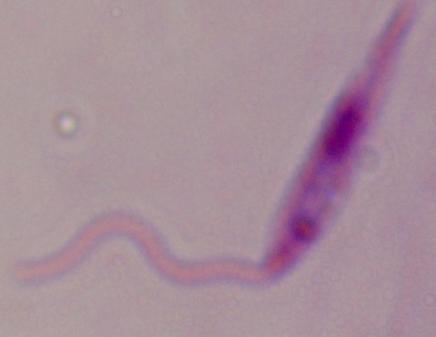

magnification = 1000x
modality = photomicrograph
identification = Leishmania